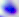
Captured at 400x magnification. Photomicrograph. Toxoplasma gondii is shown.